Comment on the morphology of the red blood cells.
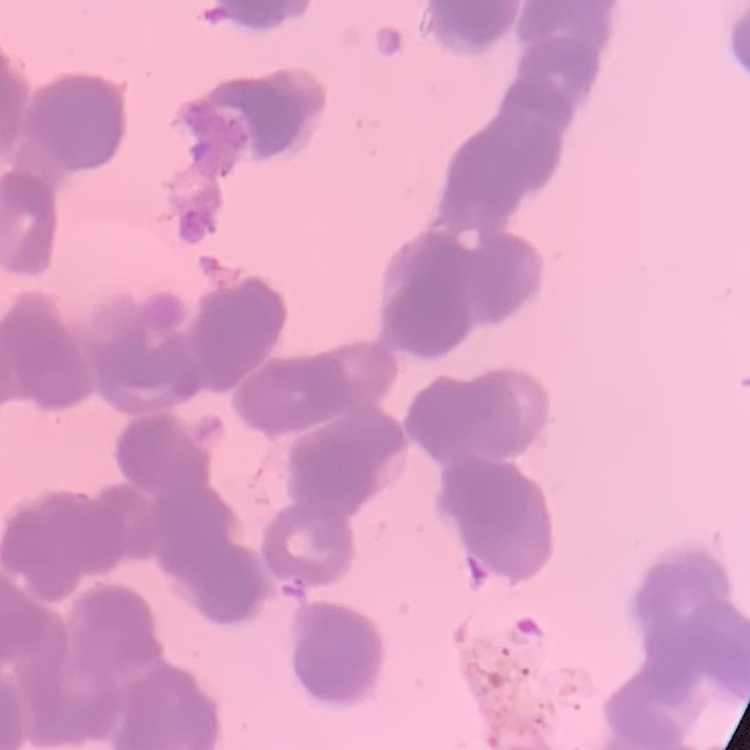
They show rouleaux formation.

Summary:
  - Stain: Field's or Giemsa
  - Image type: one tile cut from a larger photomicrograph
  - Preparation: thin blood smear